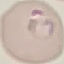 Malaria status: parasitized. Giemsa stain. Cell patch, automatically extracted from a larger field of view and resized to 64 × 64 pixels. Acquired by smartphone through the microscope eyepiece. Thin blood smear.